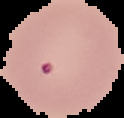
Image is 124×118 pixels. Malaria status: uninfected. From a thin blood film. The area outside the segmented cell region is set to black.